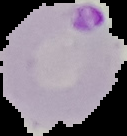
Result: Plasmodium parasites identified. Image is 127×136 pixels. From a thin blood film. Segmented cell region on a black background.